Classify this cell by malaria status.
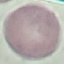

Uninfected.

Summary:
  - Preparation: thin blood film
  - Image type: cell patch, automatically extracted from a larger field of view and resized to 64 × 64 pixels
  - Capture: smartphone camera at the microscope eyepiece
  - Stain: Giemsa